Describe the morphology of the red blood cells.
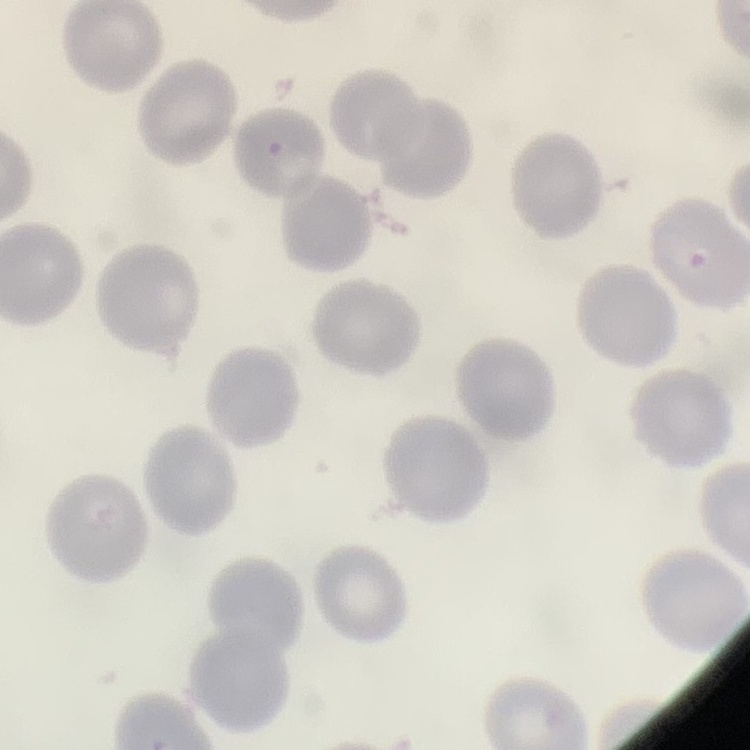

They show no rouleaux formation.

stain = Field's or Giemsa
preparation = thin peripheral smear
image type = square crop of a larger photomicrograph